Name the parasite shown.
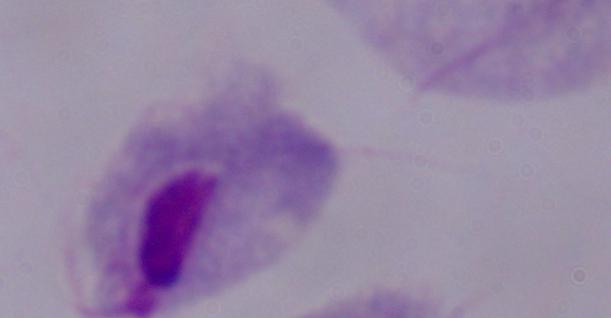
This is a trichomonad.

Captured at 1000x magnification. Photomicrograph.